Give the position of every Plasmodium parasite.
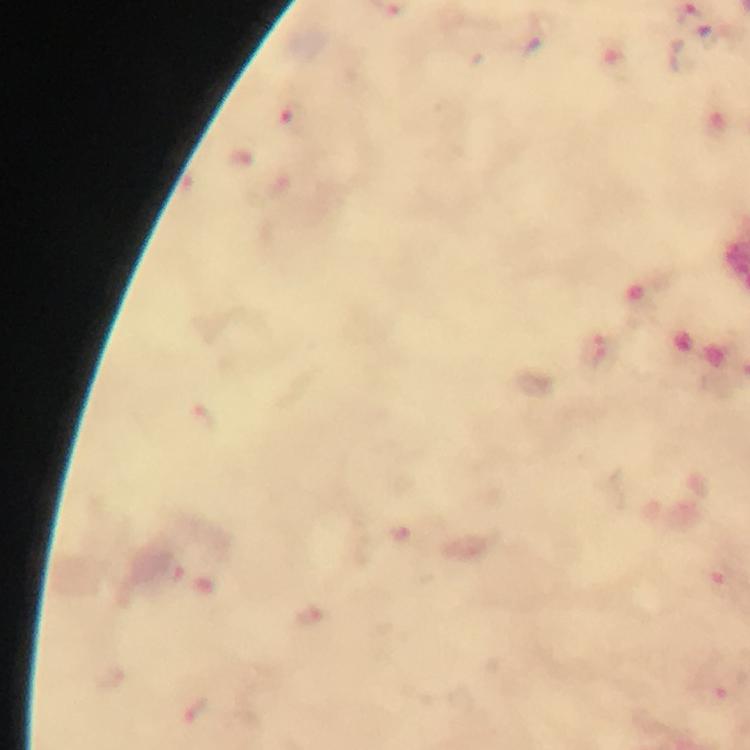
Approximate object centers, in pixels from the top-left corner.
Plasmodium parasites: (x=291, y=117), (x=592, y=352), (x=203, y=418), (x=401, y=531), (x=168, y=573), (x=717, y=576), (x=306, y=617), (x=715, y=693), (x=196, y=711).

immersion_oil: applied
preparation: thick blood film
capture: smartphone mounted on the microscope
magnification: 100x
image_size: 750×750 pixels
context: from a diagnostic examination for malaria
stain: Giemsa
cropped_from: a single field of view